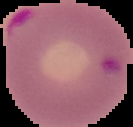
preparation = thin blood film
image type = segmented cell region on a black background
image size = 133×127 pixels
malaria status = parasitized